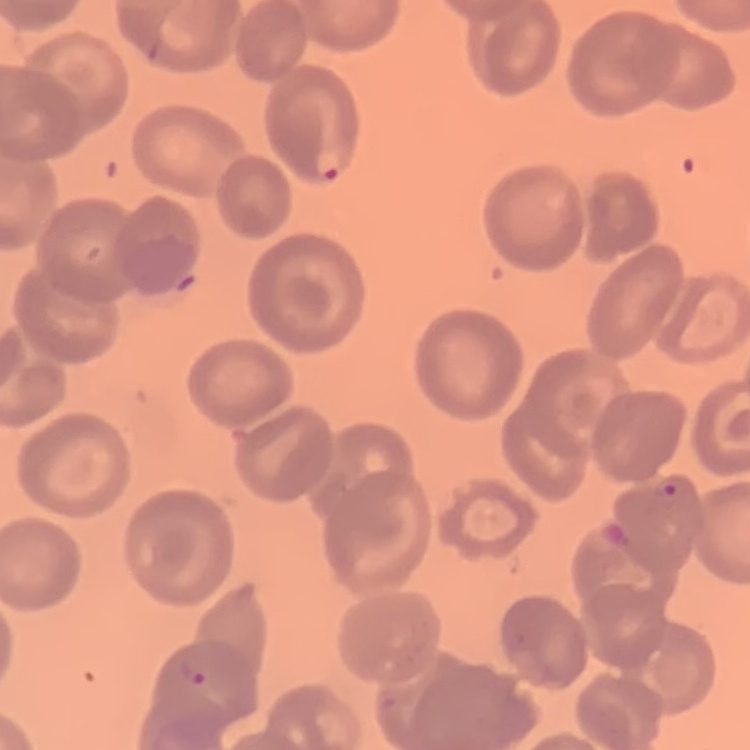

The erythrocytes exhibit no rouleaux formation. Thin peripheral smear. Stained with either Field's or Giemsa. Square crop of a larger photomicrograph.